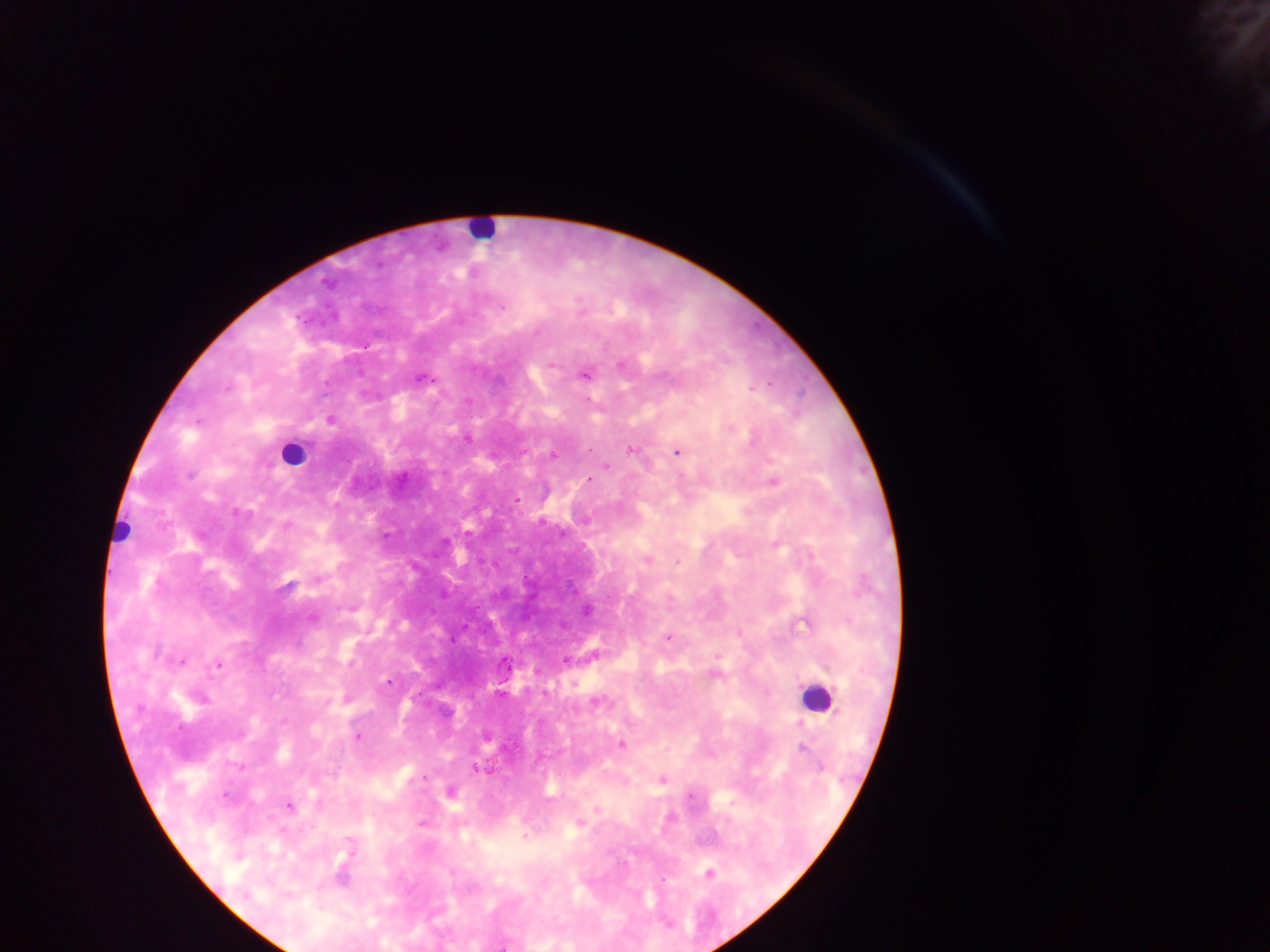 Approximate centers as x y in pixels. Leukocyte locations: 481 230; 292 454; 121 531; 816 696. Plasmodium parasite locations: 326 282; 502 307; 537 332; 553 365; 584 374; 330 420; 197 421; 730 428; 630 450; 678 452; 553 455; 606 467; 189 476; 589 480; 774 483; 516 500; 236 513; 286 526; 561 533; 647 561; 677 562; 318 579; 288 584; 587 611; 310 617; 668 638; 566 660; 182 661; 505 663; 216 664; 716 675; 388 682; 595 703; 357 737; 622 745; 803 747; 478 769; 425 777; 663 779; 451 791; 225 796; 690 796; 289 807; 597 809; 421 823; 579 824; 709 874; 664 880. Thick blood film. One field of view. Collected in Ghana. Photographed through a microscope with a mobile-phone camera. Image is 1270×952 pixels.